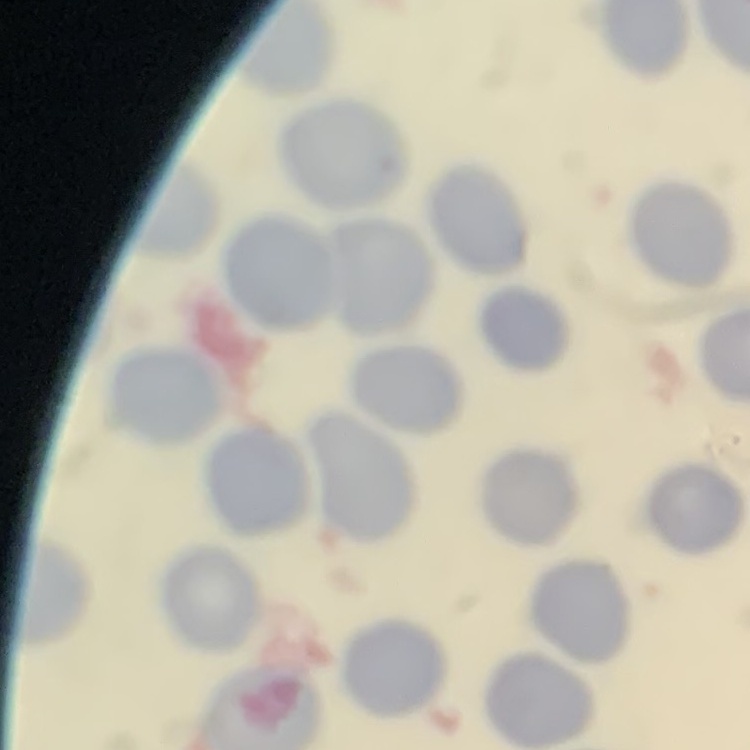

The red blood cells exhibit no rouleaux formation. Stained with either Field's or Giemsa. Thin blood film. One tile cut from a larger photomicrograph.